Identify the parasite.
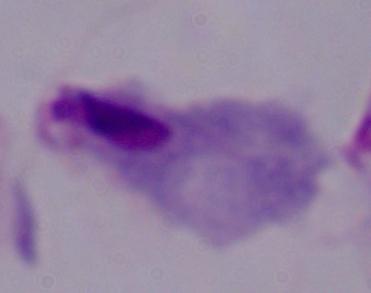
A trichomonad.

Micrograph. 1000x magnification.